Outline each Plasmodium falciparum-infected red blood cell.
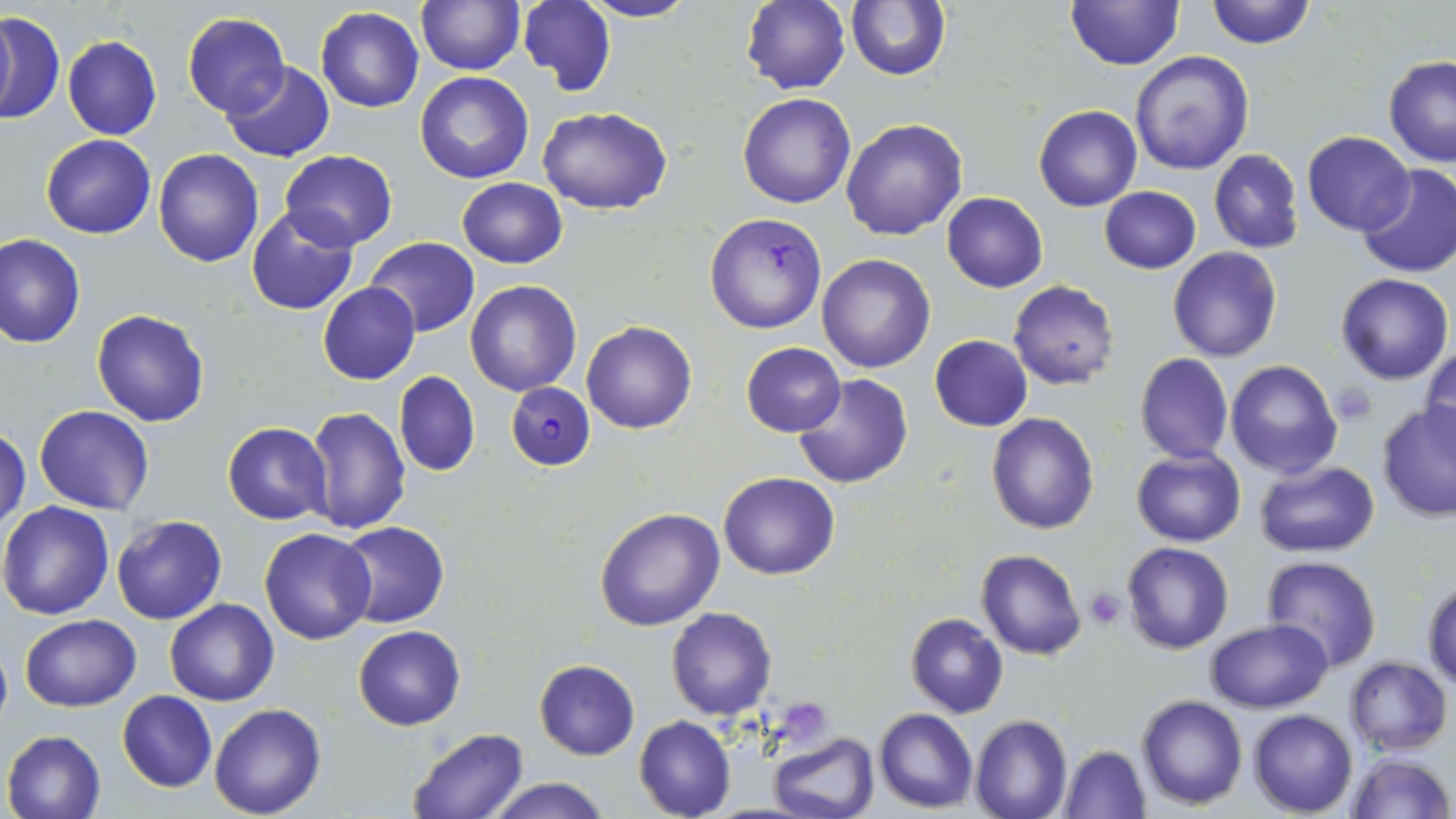
Approximate bounding boxes as named x1/y1/x2/y2 corners in pixels.
Plasmodium falciparum-infected red blood cells: (x1=705, y1=211, x2=828, y2=335), (x1=507, y1=380, x2=595, y2=470).

Uninfected red blood cell locations: (x1=518, y1=0, x2=615, y2=93), (x1=579, y1=0, x2=701, y2=23), (x1=845, y1=0, x2=951, y2=82), (x1=1064, y1=0, x2=1184, y2=71), (x1=1203, y1=0, x2=1315, y2=49), (x1=415, y1=1, x2=523, y2=74), (x1=741, y1=1, x2=850, y2=95), (x1=316, y1=8, x2=423, y2=112), (x1=0, y1=11, x2=64, y2=125), (x1=183, y1=11, x2=290, y2=118), (x1=62, y1=35, x2=162, y2=141), (x1=1129, y1=51, x2=1254, y2=175), (x1=1383, y1=56, x2=1456, y2=166), (x1=222, y1=61, x2=334, y2=162), (x1=415, y1=72, x2=534, y2=184), (x1=737, y1=92, x2=854, y2=208), (x1=539, y1=105, x2=672, y2=213), (x1=1034, y1=105, x2=1142, y2=211), (x1=842, y1=118, x2=968, y2=239), (x1=1301, y1=131, x2=1414, y2=236), (x1=41, y1=134, x2=156, y2=239), (x1=153, y1=148, x2=264, y2=267), (x1=279, y1=149, x2=397, y2=251), (x1=1208, y1=149, x2=1305, y2=254), (x1=1357, y1=163, x2=1456, y2=277), (x1=457, y1=178, x2=567, y2=268), (x1=1099, y1=185, x2=1201, y2=273), (x1=942, y1=192, x2=1048, y2=292), (x1=245, y1=208, x2=358, y2=315), (x1=0, y1=234, x2=86, y2=348), (x1=365, y1=237, x2=480, y2=336), (x1=1168, y1=247, x2=1282, y2=364), (x1=817, y1=254, x2=936, y2=373), (x1=1334, y1=272, x2=1452, y2=384), (x1=464, y1=280, x2=582, y2=397), (x1=1009, y1=280, x2=1119, y2=389), (x1=318, y1=283, x2=420, y2=384), (x1=92, y1=309, x2=211, y2=428), (x1=582, y1=319, x2=697, y2=434), (x1=928, y1=335, x2=1033, y2=432), (x1=740, y1=342, x2=847, y2=437), (x1=1421, y1=345, x2=1456, y2=451), (x1=1134, y1=353, x2=1234, y2=463), (x1=1225, y1=359, x2=1341, y2=479), (x1=394, y1=371, x2=479, y2=477), (x1=792, y1=374, x2=912, y2=489), (x1=1377, y1=401, x2=1456, y2=522), (x1=35, y1=405, x2=155, y2=515), (x1=302, y1=406, x2=412, y2=534), (x1=986, y1=411, x2=1100, y2=534), (x1=223, y1=422, x2=332, y2=526), (x1=0, y1=425, x2=29, y2=534), (x1=1131, y1=446, x2=1246, y2=546), (x1=1255, y1=459, x2=1381, y2=557), (x1=719, y1=471, x2=839, y2=579), (x1=0, y1=500, x2=118, y2=620), (x1=594, y1=506, x2=725, y2=631), (x1=111, y1=515, x2=227, y2=625), (x1=337, y1=521, x2=450, y2=629), (x1=260, y1=527, x2=376, y2=646), (x1=1122, y1=541, x2=1233, y2=654), (x1=976, y1=550, x2=1086, y2=660), (x1=1261, y1=556, x2=1382, y2=673), (x1=1422, y1=576, x2=1456, y2=689), (x1=165, y1=598, x2=278, y2=705), (x1=667, y1=607, x2=777, y2=720), (x1=905, y1=612, x2=1008, y2=718), (x1=19, y1=613, x2=142, y2=710), (x1=1205, y1=619, x2=1332, y2=712), (x1=353, y1=626, x2=466, y2=730), (x1=1344, y1=656, x2=1452, y2=756), (x1=534, y1=659, x2=639, y2=759), (x1=117, y1=691, x2=217, y2=792), (x1=1137, y1=694, x2=1247, y2=810), (x1=209, y1=703, x2=327, y2=818), (x1=874, y1=708, x2=977, y2=812), (x1=1247, y1=709, x2=1357, y2=816), (x1=634, y1=715, x2=736, y2=819), (x1=971, y1=715, x2=1072, y2=819), (x1=403, y1=728, x2=530, y2=819), (x1=2, y1=729, x2=107, y2=819), (x1=770, y1=732, x2=878, y2=819), (x1=1058, y1=744, x2=1151, y2=818), (x1=1342, y1=751, x2=1453, y2=819), (x1=485, y1=777, x2=613, y2=819). Platelet locations: (x1=1331, y1=383, x2=1377, y2=426), (x1=1084, y1=586, x2=1128, y2=630), (x1=784, y1=694, x2=828, y2=743). Slide-level diagnosis: Plasmodium falciparum. 1000x magnification. One field of a larger specimen. Thin blood film. May-Grünwald-Giemsa stain. Image is 1456×819 pixels. Optical microscopy.